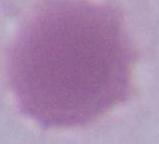

identification = erythrocyte
modality = micrograph
magnification = 1000x